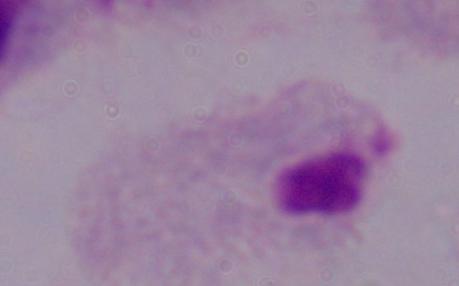
Micrograph. A trichomonad is seen. 1000x magnification.